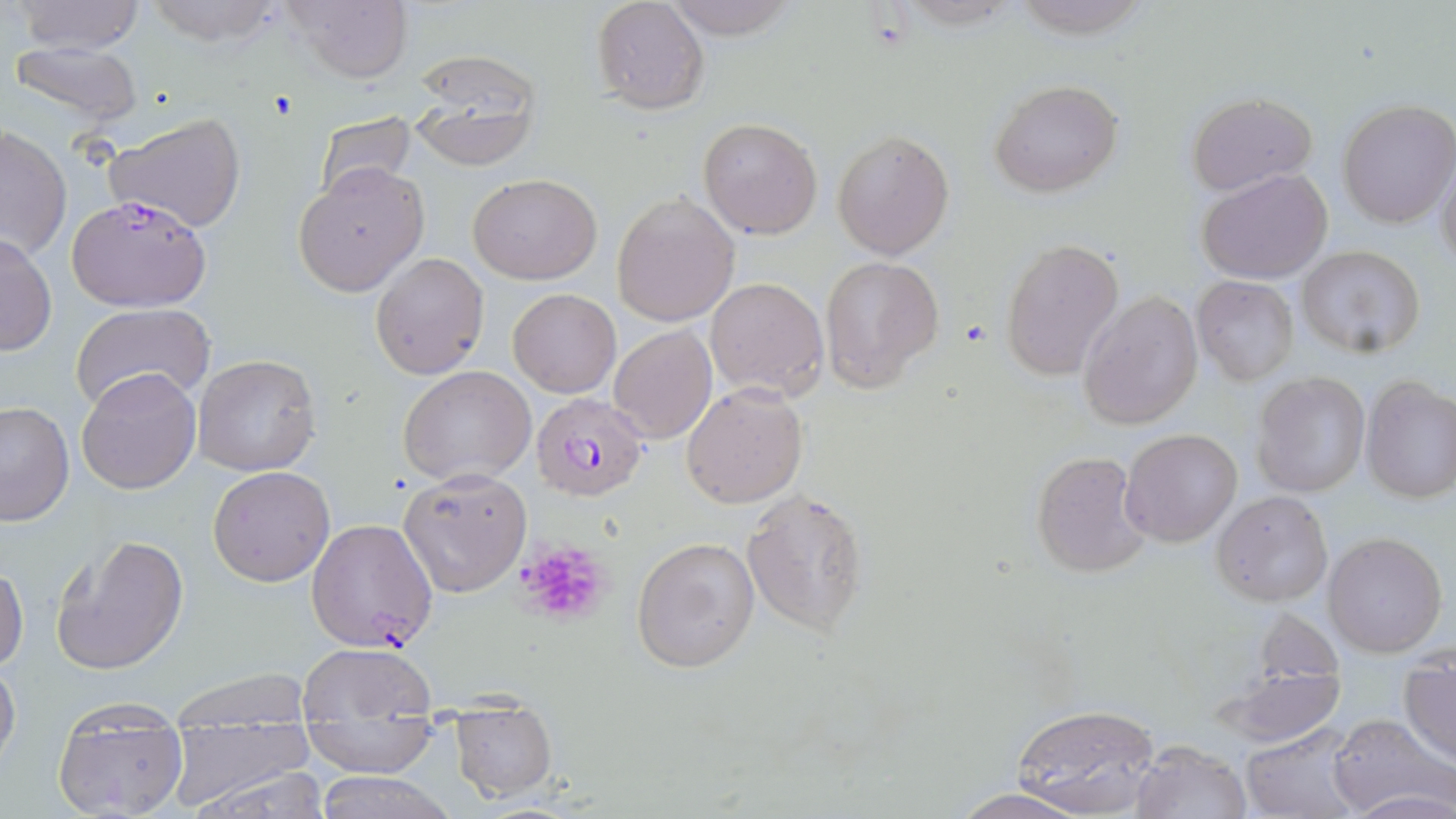

slide-level diagnosis = Plasmodium falciparum
preparation = thin blood smear
uninfected red blood cell locations = approximate bounding boxes as [x1, y1, x2, y2] in pixels: [10, 0, 148, 55], [138, 0, 291, 46], [662, 0, 800, 41], [282, 1, 414, 85], [590, 1, 710, 115], [6, 39, 145, 128], [405, 52, 543, 169], [989, 78, 1123, 197], [1188, 92, 1315, 197], [1336, 99, 1455, 229], [105, 112, 247, 234], [313, 112, 420, 203], [698, 116, 823, 239], [0, 125, 70, 264], [832, 128, 954, 259], [1435, 153, 1456, 271], [293, 165, 429, 296], [1199, 168, 1333, 283], [468, 173, 603, 284], [611, 190, 740, 327], [0, 231, 57, 357], [1001, 238, 1124, 380], [1296, 245, 1426, 358], [370, 251, 489, 378], [820, 256, 944, 392], [705, 275, 829, 402], [1193, 276, 1298, 384], [508, 287, 621, 397], [1077, 290, 1202, 432], [72, 302, 216, 412], [608, 324, 716, 444], [193, 353, 322, 477], [399, 365, 535, 485], [76, 368, 203, 494], [1253, 373, 1370, 499], [1361, 377, 1456, 503], [681, 382, 808, 508], [0, 401, 74, 527], [1121, 427, 1244, 547], [1031, 448, 1150, 579], [208, 465, 336, 587], [397, 467, 531, 596], [741, 487, 870, 638], [1212, 490, 1332, 607], [51, 533, 189, 675], [1323, 533, 1448, 656], [632, 534, 761, 673], [0, 561, 28, 676], [298, 641, 437, 721], [0, 658, 21, 774], [1401, 658, 1456, 763], [1214, 665, 1348, 748], [166, 669, 317, 726], [449, 700, 557, 801], [1011, 704, 1160, 817], [52, 713, 190, 818], [1327, 714, 1450, 816], [302, 719, 439, 779], [1241, 728, 1361, 819], [166, 732, 325, 815], [1132, 741, 1250, 819], [313, 770, 455, 819], [945, 788, 1100, 819]
field of view = single
platelet locations = approximate bounding boxes as [x1, y1, x2, y2] in pixels: [266, 91, 300, 120], [516, 539, 611, 625]
magnification = 1000x
image size = 1456×819 pixels
Plasmodium falciparum-infected red blood cell locations = approximate bounding boxes as [x1, y1, x2, y2] in pixels: [65, 193, 212, 312], [533, 391, 650, 499], [306, 517, 438, 653]
stain = May-Grünwald-Giemsa
modality = optical microscopy